Assess for parasitized red blood cells.
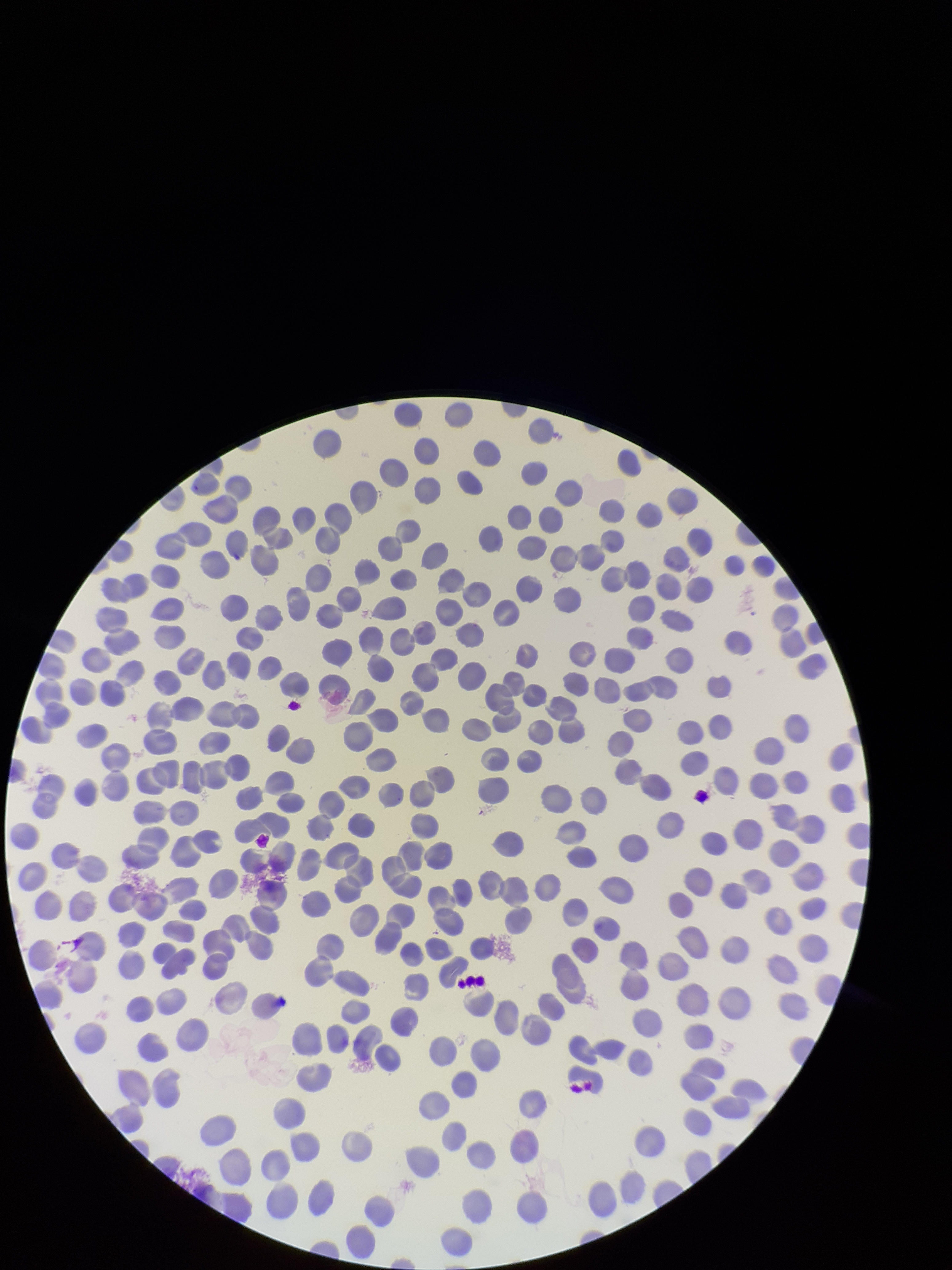
None seen.

Summary:
  - Preparation: thin
  - Species reported for this patient: Plasmodium vivax
  - Patient malaria status: positive
  - Field of view: one from this slide
  - Image size: 952×1270 pixels
  - Parasitized red blood cell count: 0
  - Red blood cell count: 325
  - Stain: Giemsa
  - Capture: smartphone photograph through the microscope eyepiece